Identify the blood parasite species.
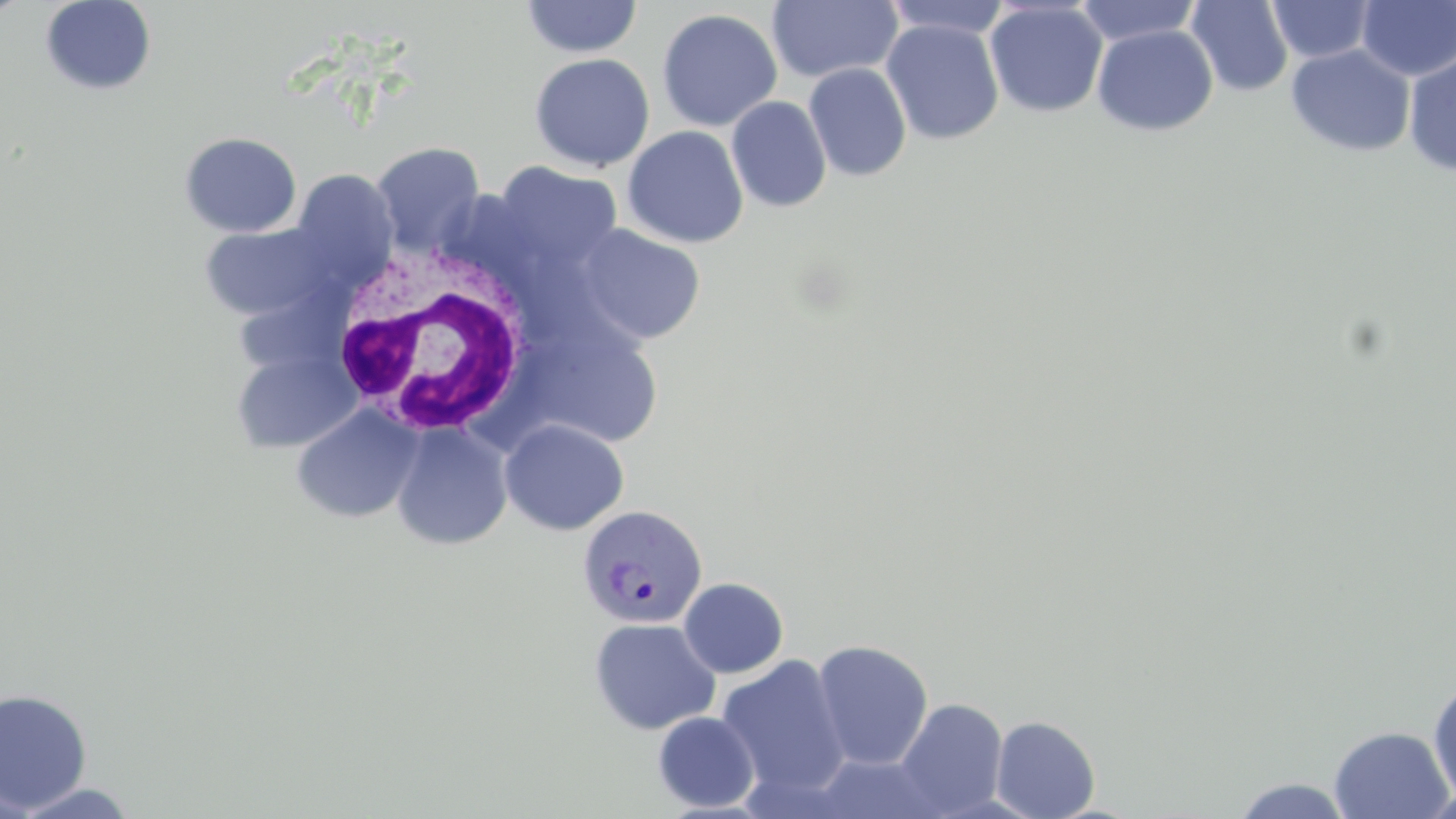

Plasmodium vivax.

Summary:
  - Coordinate format: approximate bounding boxes as (x1, y1, x2, y2) in pixels
  - Uninfected red blood cell locations: (39, 0, 157, 96), (521, 0, 643, 58), (881, 0, 1013, 40), (1074, 0, 1204, 47), (1185, 0, 1293, 97), (766, 1, 903, 83), (984, 1, 1108, 118), (1267, 1, 1377, 63), (1356, 1, 1456, 82), (657, 8, 783, 132), (880, 19, 1004, 145), (1092, 24, 1218, 136), (1286, 44, 1415, 158), (1403, 51, 1456, 177), (529, 53, 655, 172), (804, 62, 912, 182), (726, 96, 831, 213), (623, 125, 749, 248), (179, 131, 302, 238), (372, 142, 486, 255), (494, 162, 622, 273), (291, 169, 400, 285), (199, 221, 332, 321), (577, 224, 705, 345), (230, 348, 362, 453), (291, 403, 424, 524), (500, 419, 629, 536), (391, 422, 513, 551), (678, 577, 789, 679), (588, 617, 721, 735), (811, 639, 934, 771), (715, 654, 850, 798), (1428, 676, 1456, 807), (0, 688, 93, 813), (895, 697, 1008, 816), (652, 711, 760, 812), (991, 715, 1100, 819), (1329, 725, 1453, 819), (813, 752, 949, 817), (1229, 776, 1356, 818), (11, 782, 141, 819), (1418, 787, 1456, 819)
  - White blood cell locations: (330, 242, 533, 439)
  - Plasmodium vivax-infected red blood cell locations: (578, 503, 708, 629)
  - Stain: May-Grünwald-Giemsa
  - Magnification: 1000x
  - Field of view: one of a larger specimen
  - Image size: 1456×819 pixels
  - Modality: light microscopy
  - Preparation: thin blood film